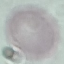
result: negative for malaria parasites
capture: smartphone camera at the microscope eyepiece
image_type: automatically extracted cell patch, resized to 64 × 64 pixels
stain: Giemsa
preparation: thin blood smear